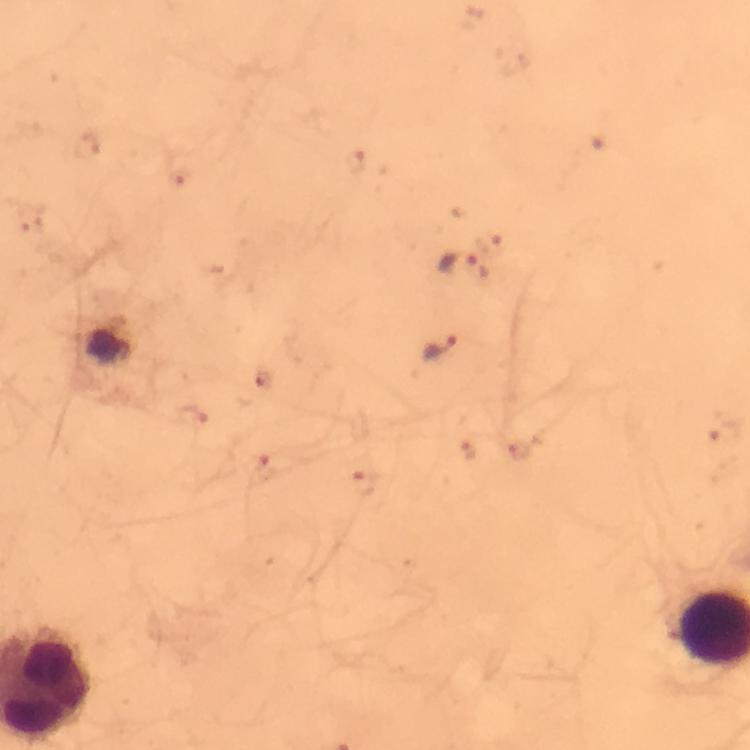

Approximate centers as [x, y] in pixels.
Summary:
  - Plasmodium parasite locations: [86, 145], [356, 160], [179, 180], [489, 239], [460, 266], [438, 348], [264, 382], [192, 417], [724, 436], [469, 447], [520, 451], [267, 467], [366, 480]
  - Capture: smartphone photograph through a microscope
  - Cropped from: a single field of view
  - Magnification: 100x
  - Image size: 750×750 pixels
  - Stain: Giemsa
  - Context: from a malaria diagnostic workup
  - Preparation: thick smear
  - Immersion oil: used